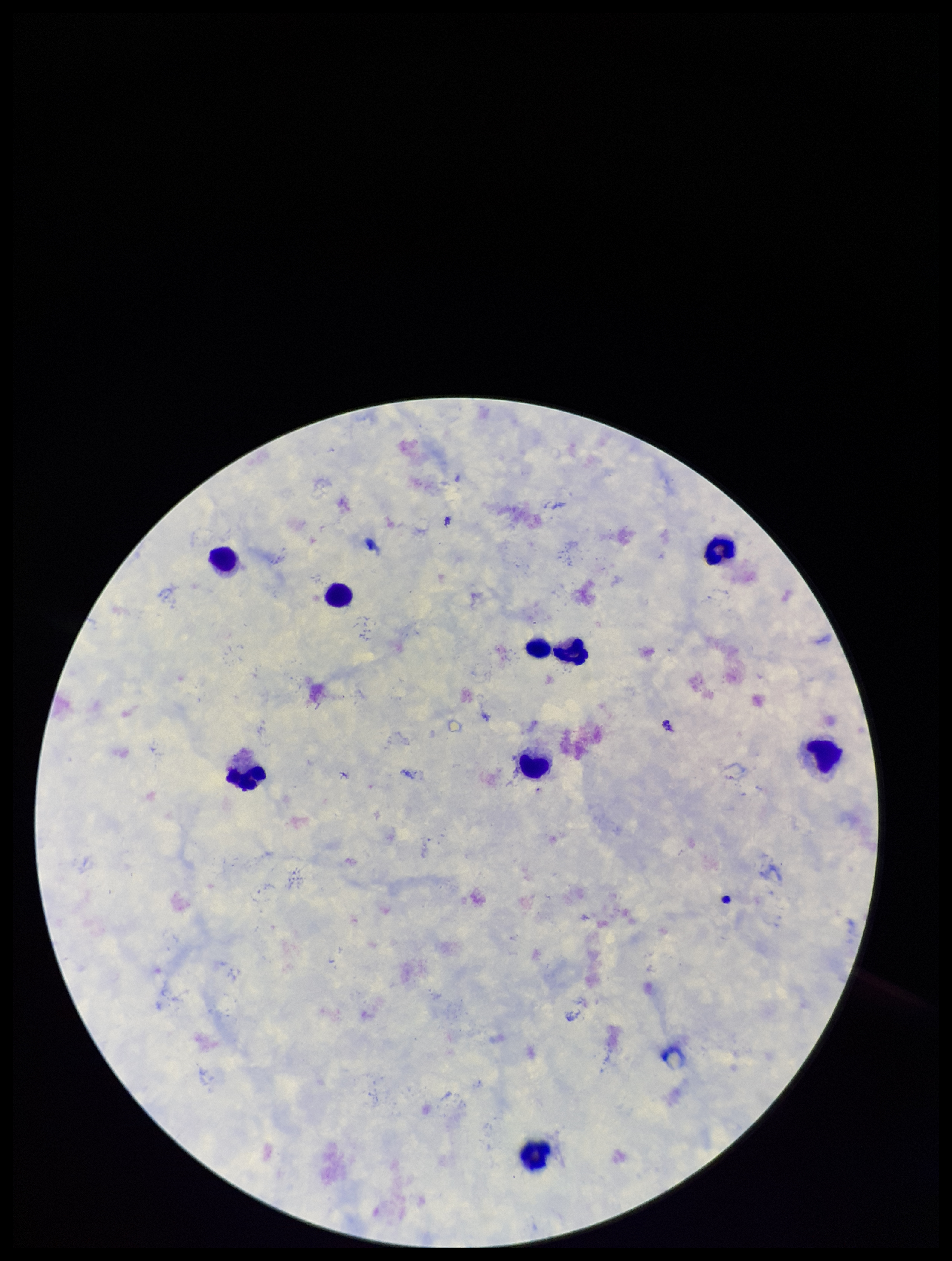

Summary:
  - Parasite count: 0
  - Stain: Giemsa
  - Patient malaria status: negative
  - Image size: 952×1261 pixels
  - Preparation: thick smear
  - Capture: smartphone photograph through the microscope eyepiece
  - Plasmodium parasites: none identified
  - Leukocyte count: 9
  - Field of view: single